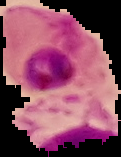 Segmented cell region on a black background. Result: malaria parasites detected. Image is 121×157 pixels. From a thin blood film.